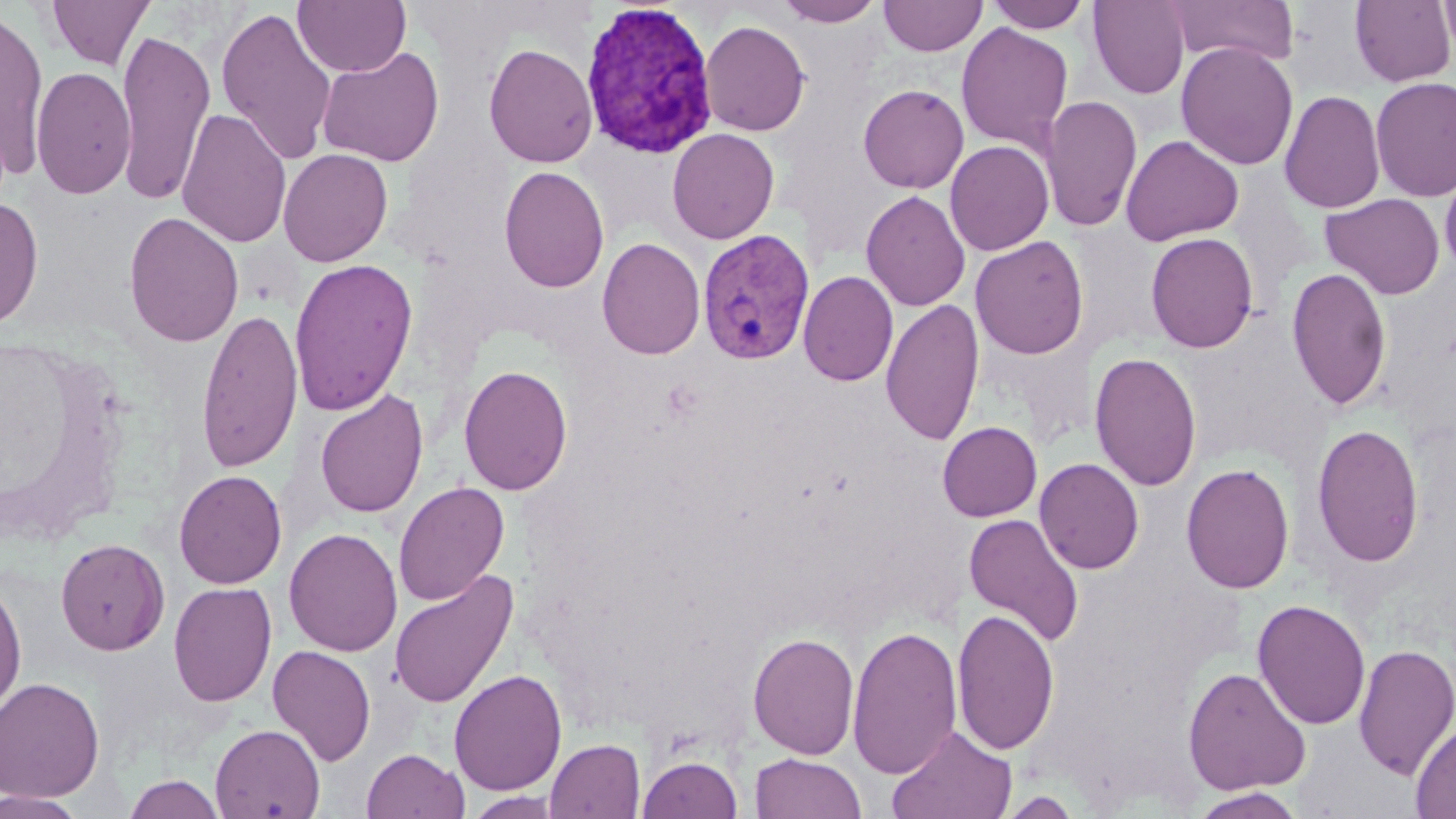
Approximate bounding boxes as (x1, y1, x2, y2) in pixels. Plasmodium vivax-infected red blood cell locations: (579, 2, 718, 159), (697, 228, 815, 365). Uninfected red blood cell locations: (46, 0, 155, 70), (293, 0, 410, 77), (775, 0, 885, 27), (879, 0, 987, 57), (987, 0, 1091, 33), (1087, 0, 1190, 99), (1163, 0, 1299, 66), (1350, 0, 1454, 87), (1439, 0, 1456, 61), (216, 7, 337, 166), (0, 9, 49, 180), (700, 20, 811, 136), (955, 22, 1074, 153), (116, 27, 216, 204), (1176, 42, 1298, 171), (483, 43, 598, 168), (316, 46, 444, 167), (31, 66, 136, 200), (1370, 76, 1456, 203), (858, 83, 969, 194), (1279, 89, 1386, 214), (1040, 94, 1142, 234), (177, 107, 292, 249), (667, 128, 779, 244), (1120, 134, 1244, 246), (945, 140, 1054, 256), (278, 148, 393, 267), (1439, 162, 1456, 280), (498, 165, 609, 292), (861, 190, 971, 311), (1321, 192, 1445, 300), (0, 196, 43, 329), (123, 211, 244, 347), (1145, 232, 1259, 353), (970, 236, 1089, 359), (596, 237, 706, 360), (288, 258, 418, 417), (1286, 266, 1392, 412), (798, 270, 898, 387), (880, 298, 984, 446), (196, 307, 304, 473), (1089, 352, 1202, 491), (458, 364, 573, 495), (314, 389, 429, 519), (937, 421, 1041, 521), (1311, 423, 1424, 567), (1034, 458, 1144, 574), (1181, 463, 1295, 594), (173, 470, 287, 589), (393, 481, 509, 606), (963, 512, 1085, 648), (283, 527, 403, 656), (55, 538, 170, 656), (388, 569, 519, 710), (0, 577, 27, 721), (168, 582, 277, 707), (1252, 599, 1371, 730), (953, 608, 1060, 756), (847, 624, 962, 781), (748, 631, 860, 760), (1353, 642, 1456, 781), (267, 645, 376, 765), (1183, 666, 1311, 795), (448, 669, 567, 796), (0, 677, 106, 803), (1410, 720, 1456, 818), (210, 724, 325, 818), (887, 724, 1017, 819), (545, 738, 645, 818), (362, 748, 469, 819), (750, 753, 865, 819), (638, 754, 743, 818), (123, 774, 226, 818), (1189, 787, 1306, 818), (0, 791, 90, 819), (465, 791, 565, 818), (997, 791, 1083, 818). Slide-level diagnosis: Plasmodium vivax. Image is 1456×819 pixels. May-Grünwald-Giemsa stain. Thin blood film. Light microscopy. Single field of view. 1000x magnification.